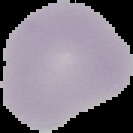
Summary:
  - Image size: 133×133 pixels
  - Image type: cell region segmented out of the field of view; surrounding area masked to black
  - Preparation: thin blood film
  - Malaria status: uninfected